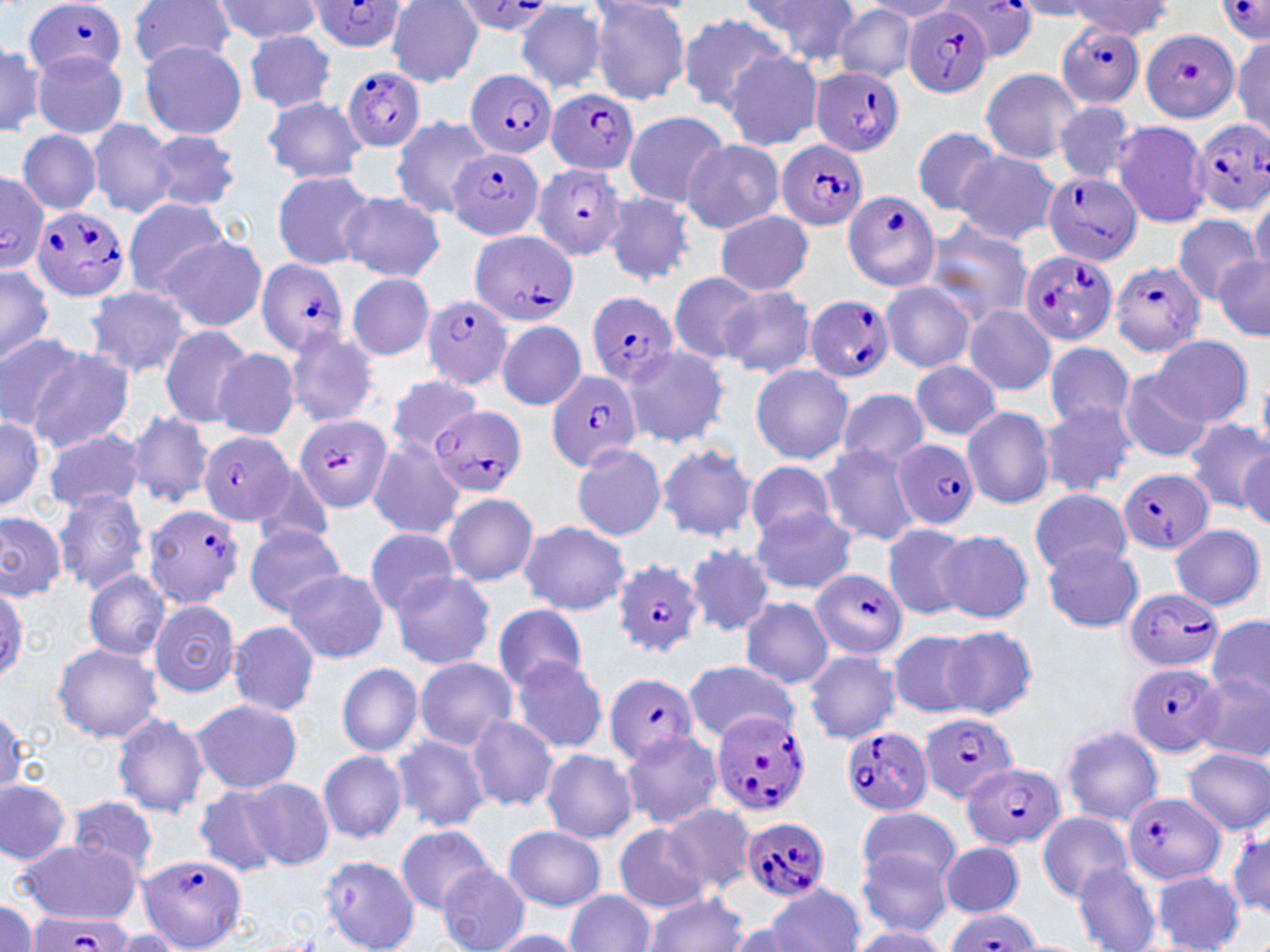

Approximate bounding boxes as (x1,y1)-(x2,y2) corner pairs in pixels. Plasmodium falciparum-infected red blood cell locations: (25,0)-(127,82), (451,0)-(556,36), (1216,0)-(1269,42), (310,2)-(408,52), (942,2)-(1041,62), (903,7)-(994,98), (1055,21)-(1146,111), (1141,28)-(1236,119), (344,66)-(426,151), (809,66)-(905,158), (468,69)-(557,159), (549,88)-(639,175), (1190,120)-(1270,216), (775,141)-(867,230), (450,148)-(545,240), (532,162)-(628,264), (1043,171)-(1140,267), (0,176)-(51,272), (842,190)-(942,292), (32,207)-(132,301), (469,230)-(577,326), (1020,248)-(1118,346), (253,257)-(350,357), (1110,258)-(1205,358), (586,289)-(681,390), (422,294)-(515,392), (804,295)-(896,383), (546,370)-(643,471), (428,406)-(526,496), (295,413)-(390,513), (199,431)-(294,527), (893,438)-(981,529), (1117,469)-(1213,554), (143,504)-(246,610), (614,560)-(707,660), (810,569)-(908,658), (1124,588)-(1223,673), (1129,663)-(1225,757), (603,670)-(699,765), (707,709)-(811,817), (919,713)-(1019,802), (839,726)-(933,816), (960,762)-(1067,849), (1120,791)-(1226,887), (740,817)-(830,901), (137,854)-(247,949), (944,908)-(1040,952), (22,914)-(138,951). Uninfected red blood cell locations: (738,0)-(863,69), (209,1)-(323,44), (588,1)-(693,106), (591,1)-(696,21), (862,1)-(964,21), (1012,1)-(1102,19), (129,2)-(240,70), (388,2)-(483,86), (1067,2)-(1173,39), (516,3)-(607,93), (834,5)-(917,81), (677,12)-(790,111), (242,29)-(337,112), (1232,37)-(1268,136), (0,42)-(45,137), (139,42)-(247,139), (721,49)-(825,152), (32,51)-(128,139), (980,67)-(1082,165), (262,95)-(368,185), (1052,101)-(1139,185), (622,110)-(731,205), (389,116)-(491,219), (86,118)-(179,220), (1111,120)-(1210,229), (912,125)-(1003,216), (17,129)-(102,214), (146,130)-(241,213), (682,138)-(784,233), (955,149)-(1060,245), (271,169)-(376,269), (339,191)-(445,282), (603,192)-(697,286), (1246,192)-(1270,280), (123,197)-(231,296), (714,210)-(814,296), (1172,214)-(1262,304), (920,219)-(1033,328), (162,237)-(266,332), (1214,254)-(1270,342), (0,264)-(53,367), (347,273)-(436,361), (667,273)-(764,364), (878,280)-(977,373), (720,285)-(816,380), (83,286)-(194,380), (962,305)-(1056,396), (495,319)-(586,411), (158,325)-(256,430), (283,329)-(381,427), (0,330)-(84,434), (1150,335)-(1254,426), (1043,341)-(1136,431), (23,345)-(134,451), (621,345)-(732,448), (213,347)-(301,441), (910,359)-(1001,441), (749,364)-(854,463), (1117,369)-(1213,464), (385,376)-(483,456), (837,387)-(929,468), (1038,401)-(1138,496), (961,404)-(1055,509), (125,411)-(215,509), (0,412)-(47,515), (1182,417)-(1268,513), (42,428)-(144,513), (367,435)-(465,539), (570,443)-(666,541), (816,443)-(922,546), (655,444)-(757,542), (1238,450)-(1270,526), (745,460)-(837,538), (251,465)-(337,550), (53,487)-(151,594), (1029,488)-(1131,575), (441,492)-(539,586), (748,505)-(857,594), (0,511)-(67,599), (517,521)-(631,616), (883,522)-(971,621), (243,524)-(347,615), (1170,525)-(1266,611), (362,526)-(461,613), (934,529)-(1034,623), (1042,541)-(1145,632), (685,543)-(775,637), (282,568)-(388,663), (83,569)-(171,659), (389,570)-(497,670), (0,577)-(27,691), (740,597)-(834,688), (148,598)-(241,698), (493,603)-(589,694), (1208,616)-(1270,703), (228,621)-(320,716), (940,626)-(1038,720), (885,629)-(986,718), (52,642)-(163,743), (802,649)-(901,744), (509,656)-(609,754), (414,657)-(519,750), (337,662)-(425,756), (681,662)-(798,740), (1194,670)-(1270,764), (190,697)-(303,795), (0,707)-(26,797), (109,710)-(211,817), (465,714)-(559,811), (1060,726)-(1164,825), (619,729)-(724,830), (391,735)-(489,833), (540,748)-(638,844), (1182,749)-(1269,835), (317,750)-(408,843), (242,777)-(335,868), (0,779)-(75,866), (192,785)-(286,877), (66,796)-(161,877), (660,803)-(756,896), (859,805)-(961,887), (1038,810)-(1131,902), (1227,816)-(1270,924), (395,824)-(493,914), (613,824)-(709,912), (503,825)-(607,911), (17,838)-(139,923), (940,839)-(1024,918), (855,849)-(954,939), (317,855)-(419,951), (1071,862)-(1162,952), (437,863)-(530,952), (1152,870)-(1245,952), (767,883)-(866,952), (565,889)-(657,952), (641,893)-(749,952), (0,897)-(40,951), (722,918)-(817,952), (848,927)-(950,951), (109,929)-(185,950), (483,930)-(588,951). Slide-level diagnosis: Plasmodium falciparum. Thin blood smear. Captured at 1000x magnification. May-Grünwald-Giemsa stain. Image is 1270×952 pixels. One field of a larger specimen. Light microscopy.